State which cell type is depicted.
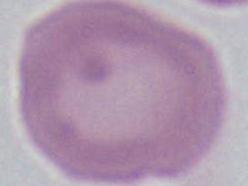

This is an erythrocyte.

modality = micrograph
magnification = 1000x